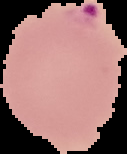
result = malaria parasites identified
image size = 127×154 pixels
preparation = thin blood smear
image type = segmented cell region with the area outside set to black